Locate every uninfected red blood cell.
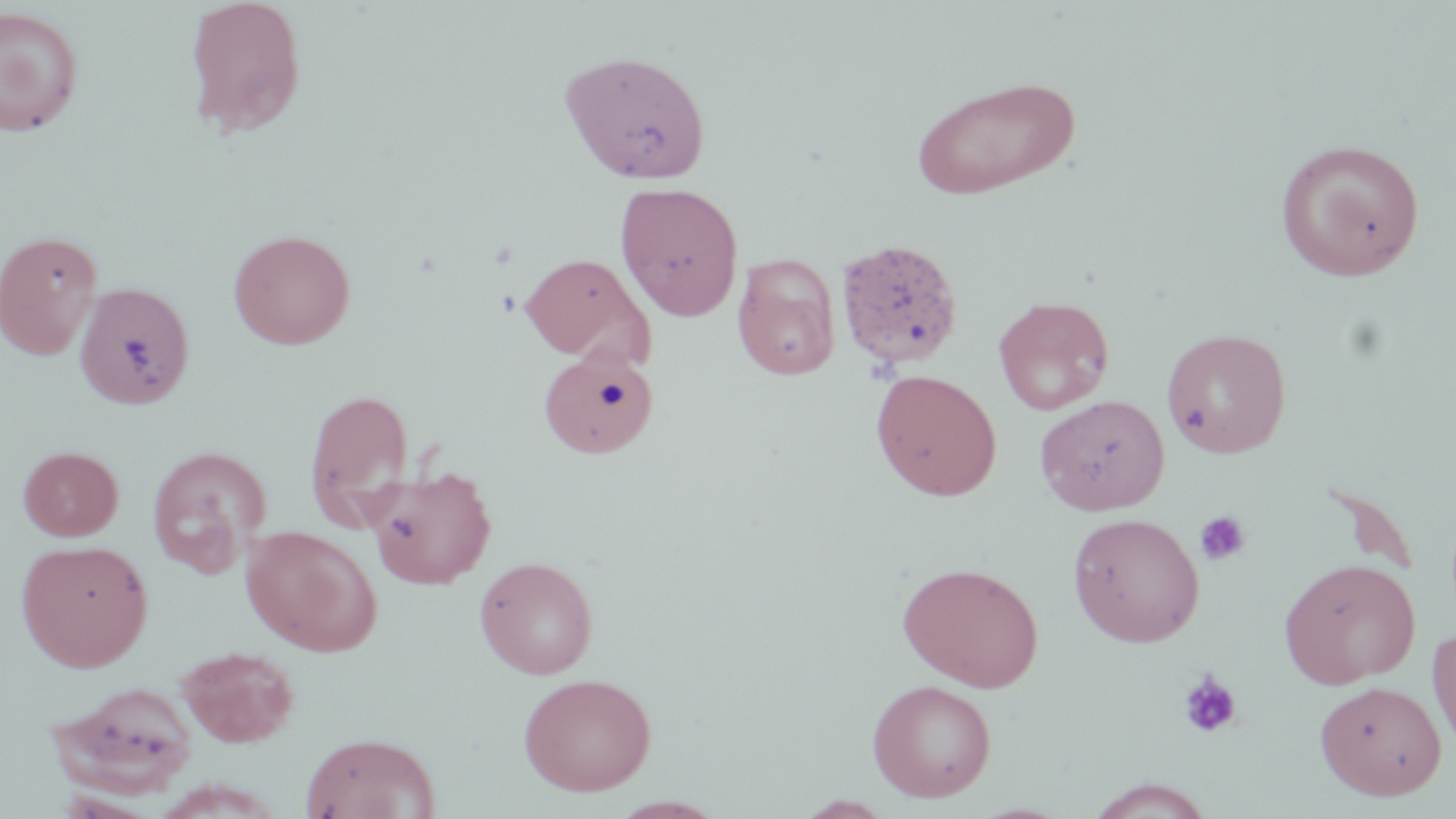
Approximate bounding boxes as [x1, y1, x2, y2] in pixels.
Uninfected red blood cells: [183, 0, 308, 139], [0, 5, 84, 136], [559, 50, 712, 184], [910, 75, 1080, 201], [1276, 138, 1425, 282], [614, 181, 744, 321], [228, 228, 355, 349], [0, 230, 103, 360], [836, 239, 964, 376], [519, 253, 654, 365], [732, 253, 841, 380], [74, 281, 195, 409], [993, 295, 1115, 415], [1160, 328, 1292, 458], [537, 350, 659, 457], [870, 370, 1002, 501], [303, 387, 415, 529], [1034, 395, 1170, 515], [146, 445, 271, 579], [18, 446, 123, 540], [364, 466, 496, 589], [1067, 512, 1205, 647], [241, 525, 382, 656], [16, 539, 153, 671], [474, 556, 598, 679], [1278, 558, 1421, 688], [896, 561, 1044, 692], [1427, 625, 1456, 756], [177, 646, 300, 748], [518, 672, 657, 796], [866, 679, 997, 803], [49, 680, 199, 799], [1315, 681, 1447, 800], [300, 732, 440, 819], [1085, 778, 1216, 818].

slide_level_diagnosis: negative for blood parasites
platelet_locations: 'approximate bounding boxes as [x1, y1, x2, y2] in pixels: [1193, 510, 1251, 566], [1177, 670, 1243, 739]'
modality: light microscopy
preparation: thin blood film
field_of_view: single
magnification: 1000x
stain: May-Grünwald-Giemsa
image_size: 1456×819 pixels